Assess the morphology of the erythrocytes.
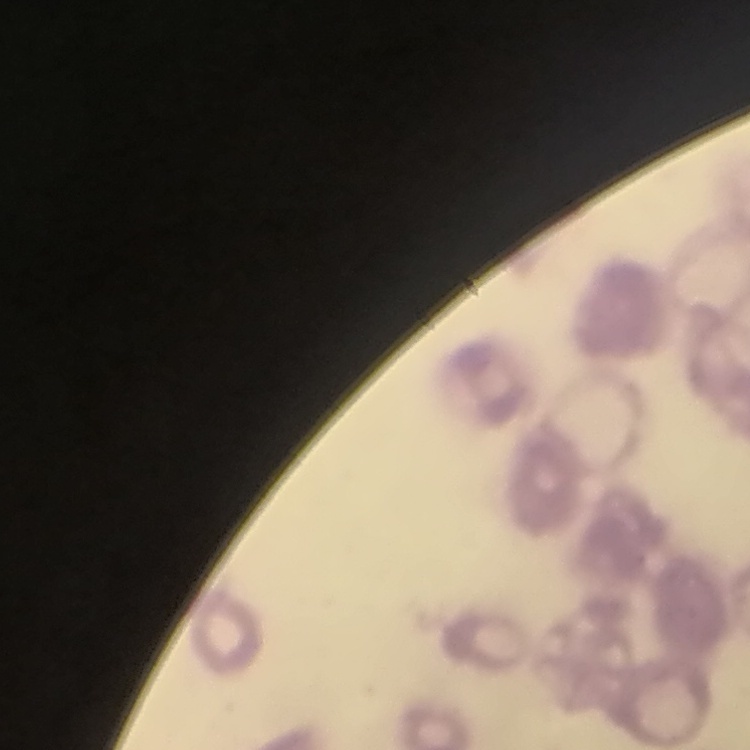
They show rouleaux formation.

{
  "preparation": "thin blood smear",
  "stain": "Field's or Giemsa",
  "image_type": "square crop of a larger photomicrograph"
}